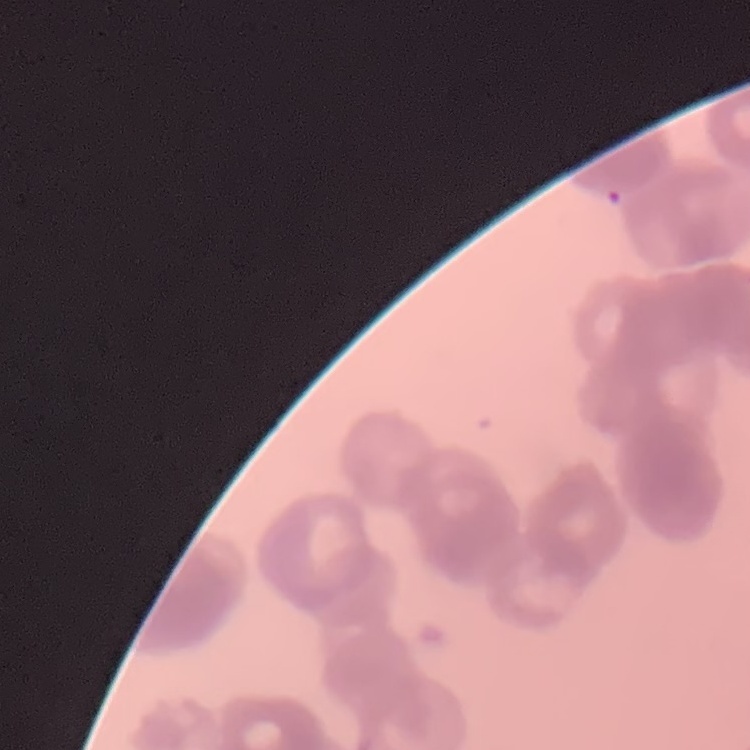 The red blood cells exhibit rouleaux formation. Stained with either Field's or Giemsa. One tile cut from a larger photomicrograph. Thin blood smear.